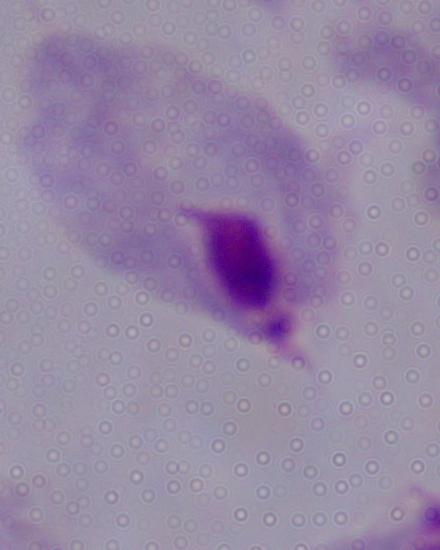

magnification = 1000x
identification = trichomonad
modality = photomicrograph